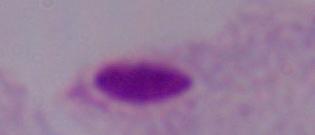

identification: trichomonad
modality: photomicrograph
magnification: 1000x